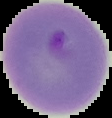

Image is 112×118 pixels. From a thin blood film. Segmented cell region on a black background. Malaria status: parasitized.